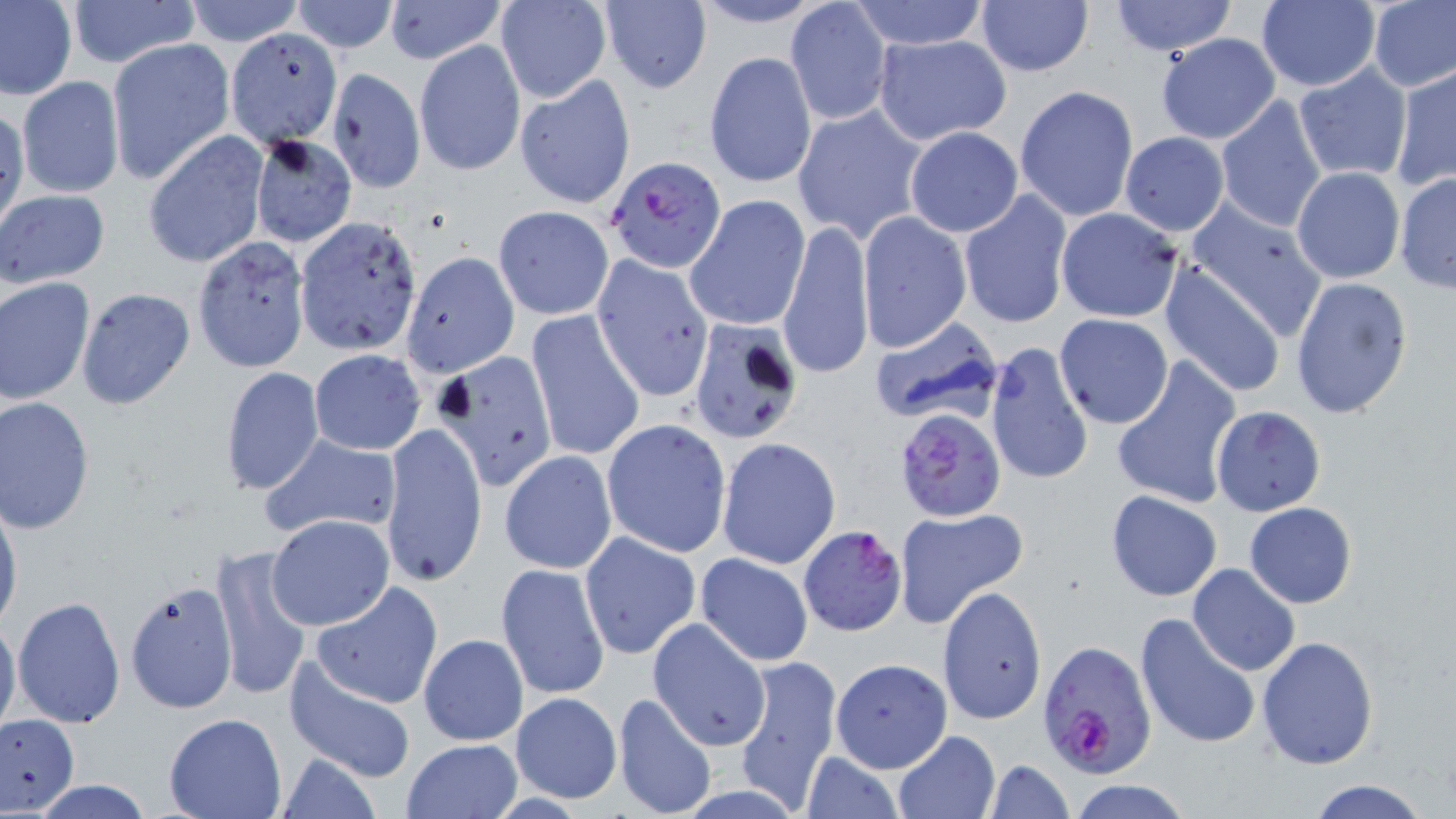

Plasmodium falciparum-infected red blood cell locations = approximate bounding boxes as named x1/y1/x2/y2 corners in pixels: (x1=603, y1=158, x2=727, y2=273), (x1=895, y1=406, x2=1005, y2=524), (x1=796, y1=523, x2=905, y2=637), (x1=1038, y1=639, x2=1159, y2=776)
slide-level diagnosis = Plasmodium falciparum
uninfected red blood cell locations = approximate bounding boxes as named x1/y1/x2/y2 corners in pixels: (x1=0, y1=0, x2=77, y2=101), (x1=66, y1=0, x2=200, y2=68), (x1=288, y1=0, x2=399, y2=53), (x1=383, y1=0, x2=508, y2=64), (x1=599, y1=0, x2=712, y2=95), (x1=683, y1=0, x2=833, y2=29), (x1=847, y1=0, x2=994, y2=49), (x1=1109, y1=0, x2=1238, y2=55), (x1=1256, y1=0, x2=1381, y2=92), (x1=1367, y1=0, x2=1456, y2=92), (x1=178, y1=1, x2=307, y2=47), (x1=785, y1=1, x2=892, y2=127), (x1=976, y1=2, x2=1094, y2=77), (x1=495, y1=3, x2=610, y2=103), (x1=225, y1=29, x2=343, y2=148), (x1=872, y1=33, x2=1013, y2=146), (x1=1156, y1=33, x2=1282, y2=144), (x1=413, y1=38, x2=526, y2=178), (x1=108, y1=39, x2=236, y2=184), (x1=705, y1=52, x2=817, y2=189), (x1=1292, y1=63, x2=1415, y2=185), (x1=1391, y1=65, x2=1455, y2=192), (x1=326, y1=67, x2=426, y2=194), (x1=514, y1=74, x2=636, y2=210), (x1=15, y1=76, x2=126, y2=199), (x1=1015, y1=85, x2=1140, y2=222), (x1=1215, y1=95, x2=1328, y2=232), (x1=0, y1=103, x2=27, y2=237), (x1=793, y1=104, x2=929, y2=243), (x1=904, y1=126, x2=1023, y2=237), (x1=1119, y1=131, x2=1230, y2=236), (x1=144, y1=132, x2=271, y2=269), (x1=249, y1=134, x2=356, y2=247), (x1=1290, y1=166, x2=1406, y2=284), (x1=1394, y1=172, x2=1456, y2=293), (x1=1, y1=189, x2=110, y2=288), (x1=958, y1=189, x2=1072, y2=328), (x1=685, y1=194, x2=811, y2=331), (x1=1186, y1=199, x2=1330, y2=338), (x1=493, y1=204, x2=615, y2=320), (x1=1054, y1=206, x2=1186, y2=323), (x1=857, y1=211, x2=971, y2=353), (x1=293, y1=217, x2=422, y2=356), (x1=778, y1=218, x2=873, y2=382), (x1=191, y1=238, x2=310, y2=373), (x1=399, y1=251, x2=519, y2=377), (x1=591, y1=253, x2=715, y2=403), (x1=1159, y1=261, x2=1287, y2=398), (x1=1290, y1=273, x2=1413, y2=419), (x1=0, y1=276, x2=96, y2=406), (x1=74, y1=288, x2=193, y2=411), (x1=525, y1=307, x2=646, y2=464), (x1=1052, y1=313, x2=1174, y2=427), (x1=869, y1=316, x2=1005, y2=429), (x1=686, y1=319, x2=805, y2=445), (x1=985, y1=341, x2=1094, y2=487), (x1=309, y1=348, x2=425, y2=455), (x1=436, y1=349, x2=560, y2=492), (x1=1111, y1=358, x2=1241, y2=510), (x1=219, y1=366, x2=325, y2=496), (x1=1, y1=397, x2=97, y2=534), (x1=1211, y1=405, x2=1325, y2=516), (x1=600, y1=418, x2=732, y2=558), (x1=379, y1=423, x2=488, y2=588), (x1=259, y1=433, x2=403, y2=540), (x1=716, y1=437, x2=841, y2=569), (x1=499, y1=450, x2=616, y2=573), (x1=1105, y1=491, x2=1222, y2=601), (x1=0, y1=493, x2=22, y2=640), (x1=1245, y1=501, x2=1357, y2=608), (x1=895, y1=507, x2=1026, y2=630), (x1=267, y1=514, x2=394, y2=631), (x1=580, y1=531, x2=701, y2=660), (x1=211, y1=543, x2=315, y2=703), (x1=696, y1=554, x2=813, y2=667), (x1=496, y1=562, x2=610, y2=700), (x1=1188, y1=563, x2=1301, y2=676), (x1=310, y1=581, x2=443, y2=709), (x1=124, y1=582, x2=237, y2=715), (x1=938, y1=584, x2=1047, y2=724), (x1=11, y1=594, x2=125, y2=730), (x1=1135, y1=612, x2=1262, y2=752), (x1=0, y1=614, x2=21, y2=743), (x1=648, y1=620, x2=771, y2=751), (x1=419, y1=634, x2=528, y2=746), (x1=1257, y1=637, x2=1378, y2=770), (x1=734, y1=653, x2=843, y2=809), (x1=285, y1=657, x2=419, y2=784), (x1=829, y1=657, x2=950, y2=774), (x1=510, y1=692, x2=622, y2=803), (x1=612, y1=693, x2=718, y2=819), (x1=163, y1=711, x2=287, y2=818), (x1=0, y1=712, x2=79, y2=815), (x1=892, y1=731, x2=999, y2=818), (x1=401, y1=738, x2=522, y2=818), (x1=277, y1=751, x2=382, y2=819), (x1=800, y1=751, x2=904, y2=819), (x1=985, y1=759, x2=1074, y2=819), (x1=1306, y1=778, x2=1431, y2=819), (x1=25, y1=779, x2=161, y2=818), (x1=1067, y1=780, x2=1193, y2=818)
magnification = 1000x
modality = light microscopy
field of view = single
image size = 1456×819 pixels
preparation = thin blood smear
stain = May-Grünwald-Giemsa